Classify this cell by malaria status.
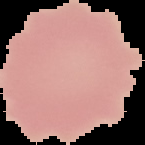
It is uninfected.

Image is 145×145 pixels. From a thin blood film. The area outside the segmented cell region is set to black.